Identify the blood parasite species.
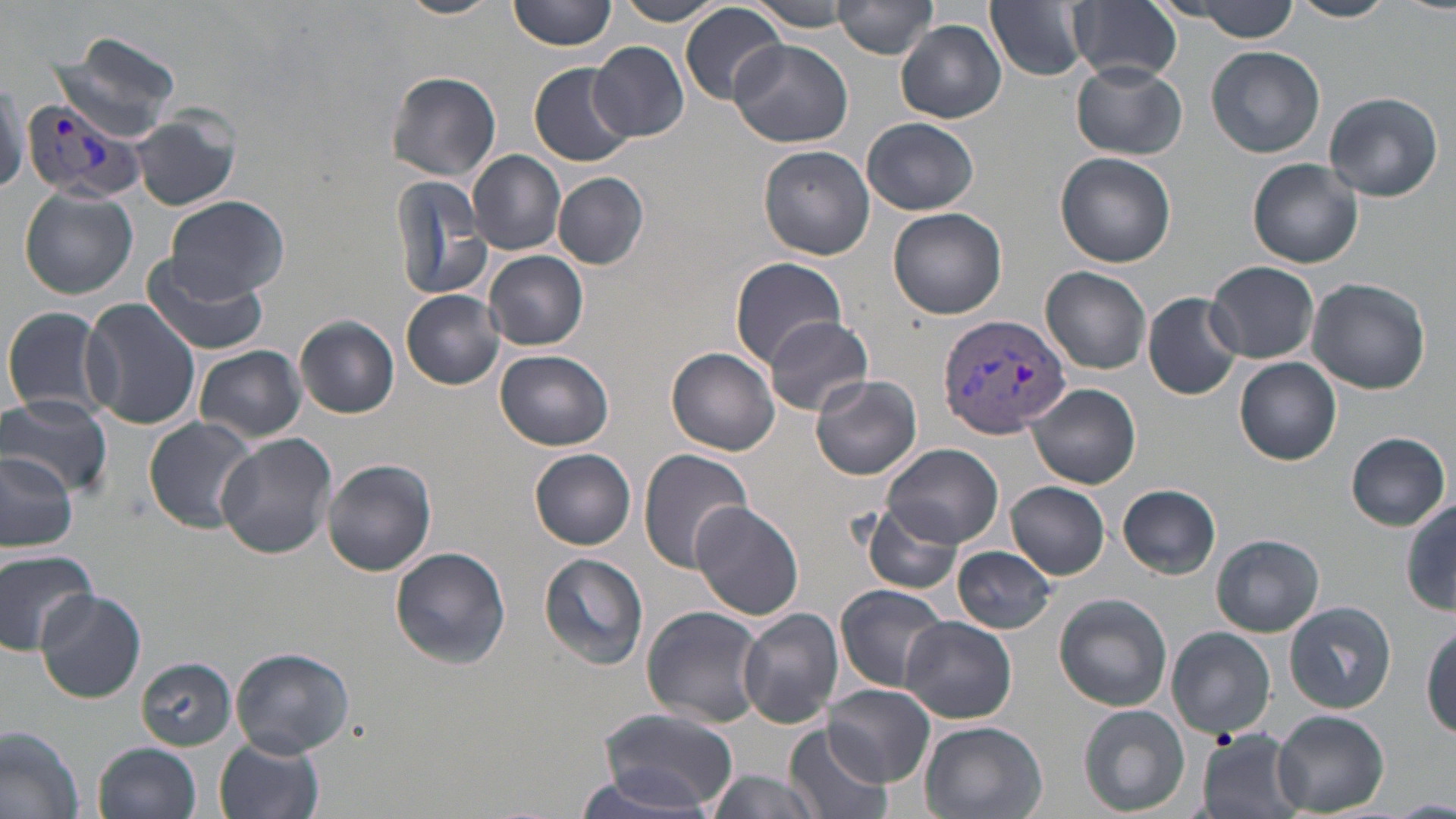
Plasmodium vivax.

magnification = 1000x
Plasmodium vivax-infected red blood cell locations = approximate bounding boxes as [x1, y1, x2, y2] in pixels: [21, 97, 149, 206], [939, 311, 1073, 438]
stain = May-Grünwald-Giemsa
modality = optical microscopy
preparation = thin blood smear
field of view = single
uninfected red blood cell locations = approximate bounding boxes as [x1, y1, x2, y2] in pixels: [395, 0, 501, 19], [509, 0, 615, 52], [613, 0, 724, 25], [834, 0, 939, 58], [1164, 0, 1308, 38], [1286, 0, 1397, 22], [748, 1, 858, 32], [985, 1, 1091, 82], [1069, 1, 1183, 85], [681, 2, 786, 105], [896, 19, 1007, 123], [52, 35, 183, 141], [730, 38, 853, 148], [589, 40, 688, 142], [1207, 46, 1326, 159], [1070, 61, 1187, 159], [529, 63, 634, 165], [384, 71, 502, 181], [1323, 91, 1444, 202], [131, 111, 240, 212], [862, 117, 980, 215], [758, 144, 876, 260], [468, 150, 566, 253], [1055, 152, 1177, 268], [1248, 159, 1363, 269], [390, 171, 496, 304], [553, 173, 649, 268], [18, 189, 138, 299], [164, 196, 291, 302], [888, 208, 1006, 319], [483, 250, 589, 351], [142, 256, 268, 356], [731, 257, 849, 365], [1208, 260, 1319, 362], [1041, 267, 1153, 375], [1306, 279, 1431, 393], [401, 290, 505, 389], [1143, 291, 1243, 400], [79, 298, 202, 431], [1, 304, 108, 420], [761, 315, 873, 417], [296, 316, 400, 418], [194, 345, 305, 443], [667, 347, 779, 455], [494, 349, 612, 450], [1234, 357, 1341, 465], [810, 374, 922, 479], [1029, 383, 1141, 488], [0, 393, 112, 499], [143, 417, 258, 533], [216, 433, 336, 559], [1345, 433, 1451, 531], [882, 443, 1004, 549], [530, 448, 638, 549], [0, 449, 75, 556], [639, 449, 754, 573], [321, 459, 437, 576], [1008, 482, 1111, 578], [1118, 484, 1222, 577], [690, 500, 804, 621], [862, 502, 965, 597], [1403, 504, 1456, 616], [1211, 534, 1324, 636], [389, 547, 512, 668], [952, 547, 1059, 635], [0, 548, 98, 655], [539, 553, 649, 667], [835, 583, 950, 692], [35, 587, 146, 703], [1054, 592, 1174, 712], [1286, 601, 1396, 713], [640, 605, 766, 726], [738, 608, 843, 728], [901, 616, 1016, 724], [1423, 626, 1456, 738], [1167, 627, 1276, 739], [229, 646, 354, 758], [139, 657, 237, 749], [824, 684, 935, 786], [1078, 705, 1191, 817], [594, 708, 740, 810], [1273, 710, 1389, 815], [918, 720, 1047, 819], [0, 724, 86, 819], [785, 725, 892, 819], [1195, 730, 1308, 819], [214, 736, 326, 819], [92, 742, 201, 819], [573, 764, 720, 817], [702, 771, 827, 819]
image size = 1456×819 pixels